Name the cell type shown.
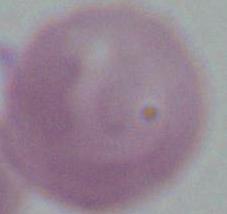

This is an erythrocyte.

Photomicrograph. 1000x magnification.